Outline each Plasmodium ovale-infected red blood cell.
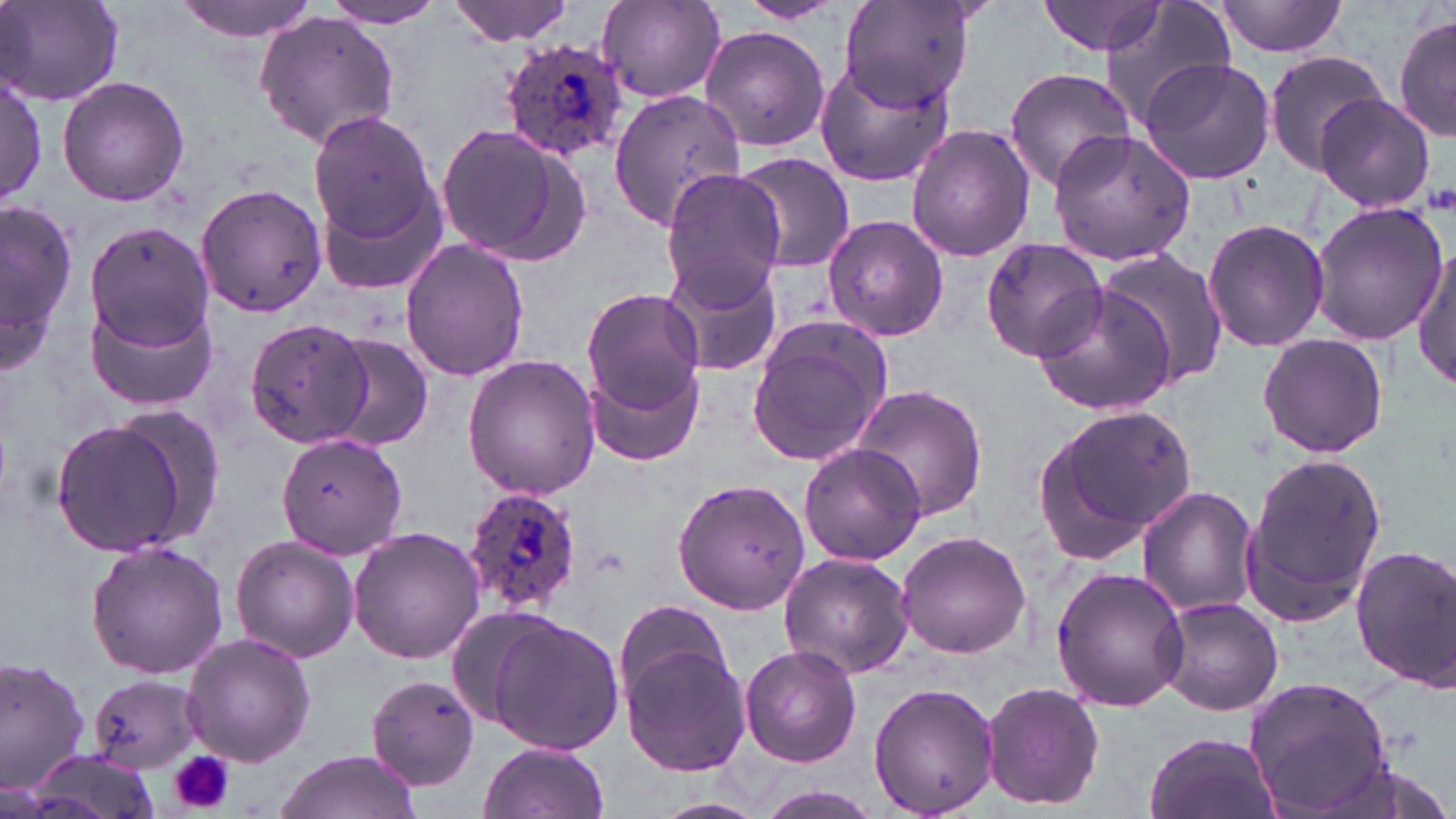
Approximate bounding boxes as (x1, y1, x2, y2) in pixels.
Plasmodium ovale-infected red blood cells: (500, 35, 632, 162), (460, 485, 583, 614).

slide-level diagnosis = Plasmodium ovale
stain = May-Grünwald-Giemsa
platelet locations = approximate bounding boxes as (x1, y1, x2, y2) in pixels: (168, 751, 234, 812)
uninfected red blood cell locations = approximate bounding boxes as (x1, y1, x2, y2) in pixels: (173, 0, 320, 40), (447, 0, 578, 44), (734, 0, 848, 25), (838, 0, 977, 112), (1039, 0, 1170, 57), (2, 1, 123, 107), (321, 1, 446, 29), (596, 1, 727, 103), (1099, 1, 1239, 127), (1213, 1, 1354, 58), (1393, 11, 1455, 142), (254, 14, 400, 148), (699, 23, 832, 153), (1262, 49, 1390, 174), (1139, 57, 1277, 186), (812, 59, 955, 189), (1003, 68, 1138, 191), (0, 71, 46, 209), (57, 76, 190, 207), (609, 90, 746, 229), (1314, 94, 1440, 213), (307, 109, 439, 246), (435, 122, 593, 264), (906, 125, 1035, 262), (1045, 127, 1197, 268), (732, 151, 854, 275), (658, 168, 786, 307), (315, 174, 450, 300), (193, 184, 327, 319), (0, 198, 76, 378), (1308, 200, 1446, 347), (823, 214, 950, 342), (1202, 217, 1330, 355), (84, 220, 216, 354), (980, 237, 1107, 361), (399, 239, 530, 381), (1413, 246, 1455, 390), (1094, 248, 1231, 389), (660, 256, 784, 378), (1029, 280, 1178, 416), (582, 288, 705, 411), (85, 290, 222, 412), (243, 316, 373, 450), (747, 318, 891, 466), (323, 333, 435, 451), (1256, 333, 1389, 460), (463, 354, 601, 499), (585, 358, 705, 467), (850, 383, 988, 521), (1037, 404, 1200, 556), (109, 407, 228, 544), (51, 418, 191, 558), (275, 430, 407, 559), (799, 443, 927, 565), (1242, 449, 1387, 623), (673, 477, 811, 613), (1136, 486, 1258, 616), (348, 527, 485, 664), (895, 529, 1032, 658), (230, 536, 361, 661), (84, 540, 228, 680), (1350, 544, 1456, 691), (778, 552, 917, 679), (1052, 566, 1189, 711), (1158, 595, 1284, 716), (614, 598, 734, 711), (482, 614, 625, 756), (181, 632, 316, 768), (620, 640, 753, 777), (740, 645, 862, 766), (0, 655, 93, 795), (364, 674, 482, 790), (89, 675, 202, 771), (1244, 677, 1396, 817), (868, 683, 999, 814), (982, 683, 1105, 810), (1144, 729, 1280, 819), (477, 740, 611, 819), (21, 750, 156, 818), (270, 751, 423, 819), (747, 785, 888, 819)
field of view = one of a larger specimen
modality = optical microscopy
magnification = 1000x
image size = 1456×819 pixels
preparation = thin blood film